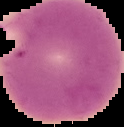

preparation: thin blood smear
image_size: 124×127 pixels
malaria_status: parasitized
image_type: segmented cell region on a black background